Describe the morphology of the erythrocytes.
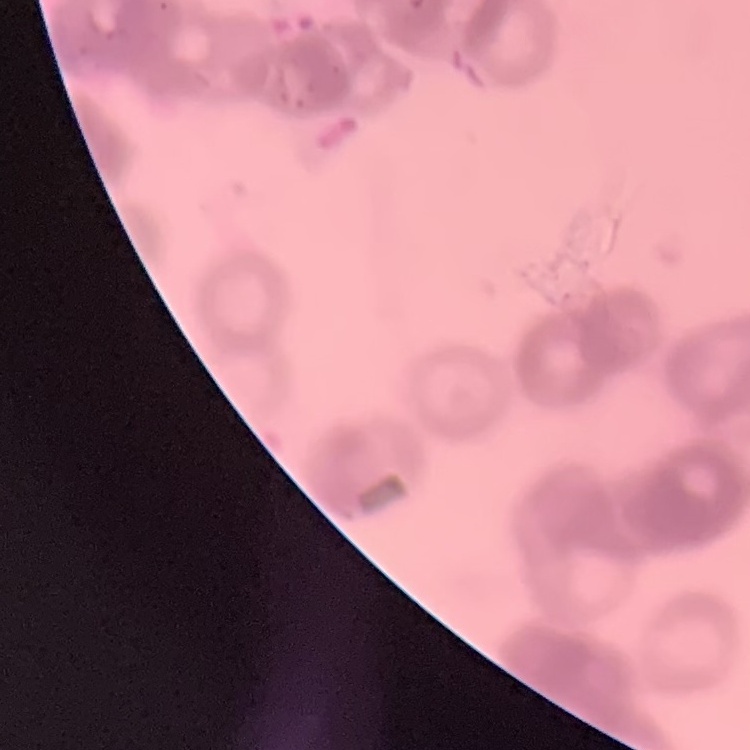

Rouleaux formation.

Square crop of a larger photomicrograph. Field's or Giemsa stain. Thin peripheral smear.